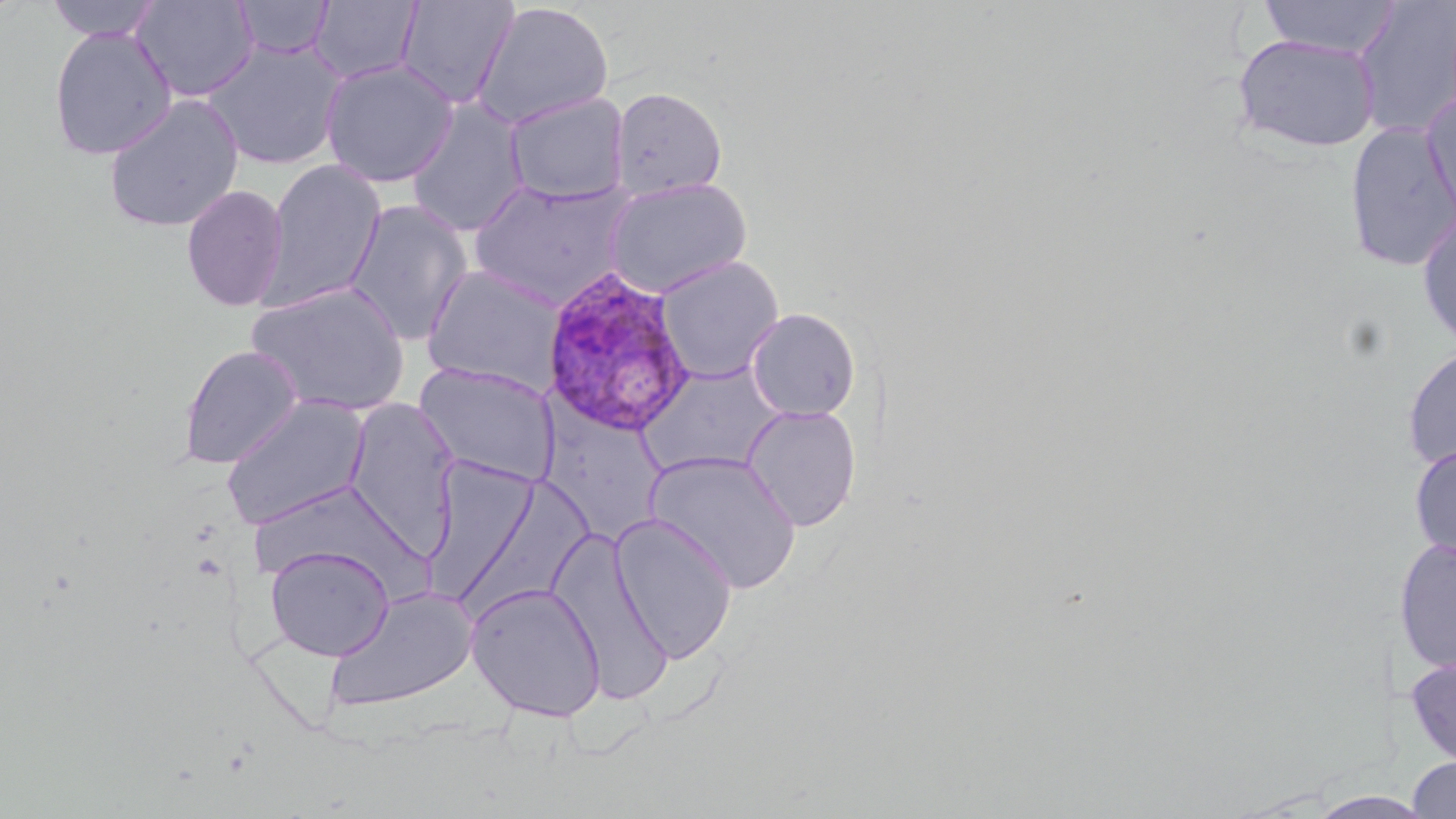

Approximate bounding boxes as named x1/y1/x2/y2 corners in pixels. Uninfected red blood cell locations: (x1=44, y1=0, x2=162, y2=41), (x1=131, y1=0, x2=258, y2=102), (x1=233, y1=0, x2=334, y2=59), (x1=309, y1=0, x2=422, y2=84), (x1=395, y1=0, x2=519, y2=109), (x1=1257, y1=0, x2=1401, y2=59), (x1=1352, y1=0, x2=1456, y2=140), (x1=472, y1=2, x2=614, y2=130), (x1=48, y1=26, x2=177, y2=161), (x1=1232, y1=33, x2=1382, y2=154), (x1=201, y1=37, x2=348, y2=171), (x1=320, y1=58, x2=458, y2=189), (x1=609, y1=86, x2=728, y2=200), (x1=1421, y1=88, x2=1456, y2=230), (x1=504, y1=91, x2=629, y2=205), (x1=103, y1=94, x2=245, y2=233), (x1=407, y1=99, x2=531, y2=237), (x1=1344, y1=121, x2=1456, y2=273), (x1=258, y1=157, x2=386, y2=313), (x1=603, y1=176, x2=753, y2=298), (x1=469, y1=177, x2=636, y2=309), (x1=180, y1=184, x2=289, y2=312), (x1=343, y1=199, x2=474, y2=346), (x1=1416, y1=209, x2=1456, y2=351), (x1=655, y1=255, x2=784, y2=384), (x1=422, y1=263, x2=570, y2=396), (x1=246, y1=281, x2=411, y2=417), (x1=746, y1=307, x2=862, y2=420), (x1=177, y1=344, x2=304, y2=469), (x1=1402, y1=345, x2=1456, y2=471), (x1=414, y1=362, x2=561, y2=488), (x1=637, y1=363, x2=785, y2=478), (x1=543, y1=388, x2=670, y2=548), (x1=220, y1=394, x2=372, y2=530), (x1=346, y1=398, x2=459, y2=552), (x1=742, y1=404, x2=862, y2=532), (x1=1409, y1=442, x2=1456, y2=559), (x1=645, y1=450, x2=803, y2=595), (x1=453, y1=473, x2=596, y2=616), (x1=251, y1=490, x2=441, y2=609), (x1=609, y1=513, x2=739, y2=663), (x1=544, y1=526, x2=675, y2=704), (x1=1393, y1=537, x2=1456, y2=676), (x1=265, y1=544, x2=393, y2=661), (x1=466, y1=582, x2=607, y2=722), (x1=324, y1=586, x2=478, y2=714), (x1=1404, y1=655, x2=1456, y2=769), (x1=1404, y1=755, x2=1456, y2=818), (x1=1305, y1=790, x2=1440, y2=818). Plasmodium ovale-infected red blood cell locations: (x1=540, y1=267, x2=697, y2=437). Slide-level diagnosis: Plasmodium ovale. Image is 1456×819 pixels. 1000x magnification. May-Grünwald-Giemsa stain. One field of a larger specimen. Thin blood film. Light microscopy.